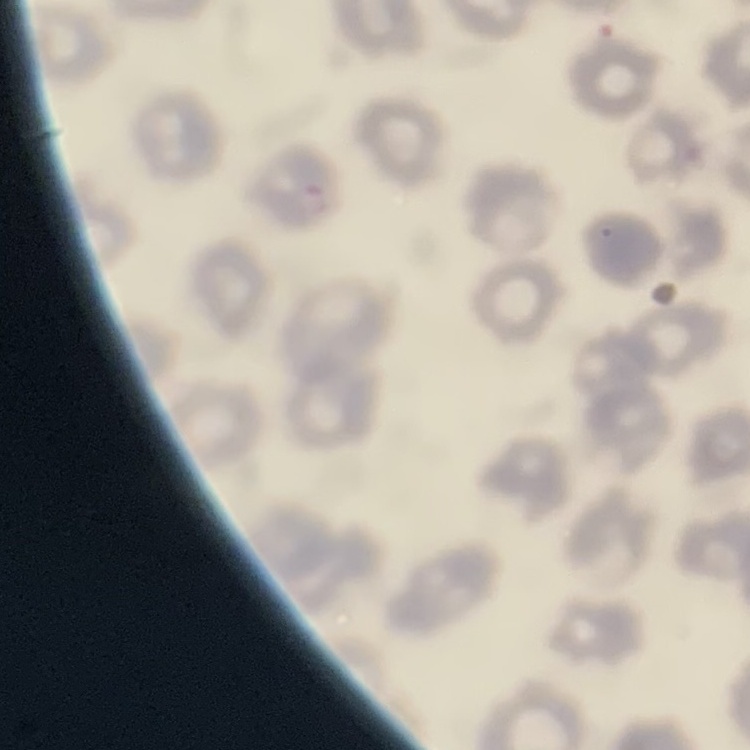
erythrocyte morphology = no rouleaux formation
stain = Field's or Giemsa
image type = square crop of a larger photomicrograph
preparation = thin peripheral smear